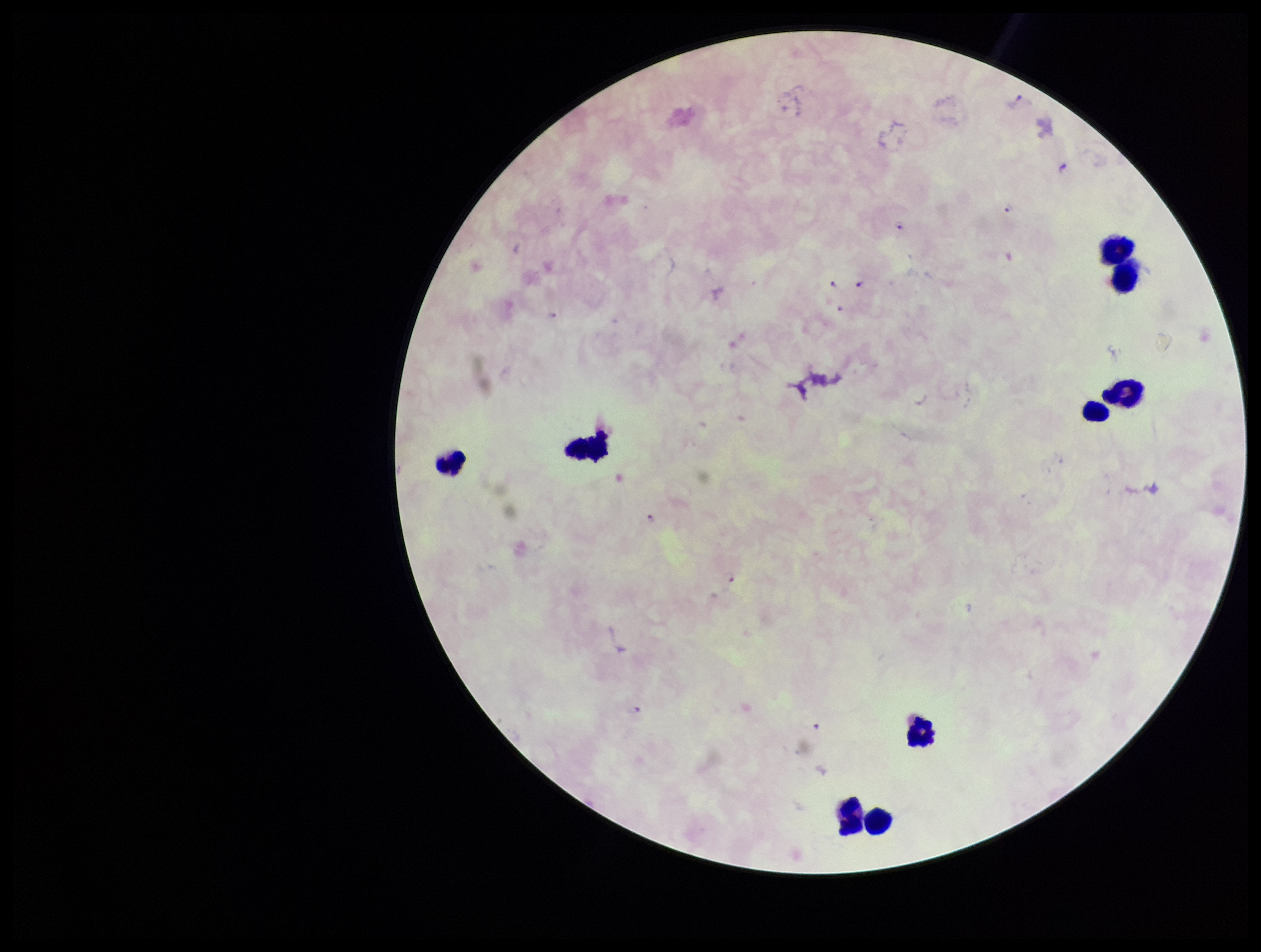
Single field of view. Patient malaria status: positive. Photographed through the microscope eyepiece with a smartphone camera. Parasite count: 12. Leukocyte count: 9. Species reported for this patient: Plasmodium falciparum. Plasmodium parasites: identified. Preparation: thick. Image is 1261×952 pixels. Giemsa stain.